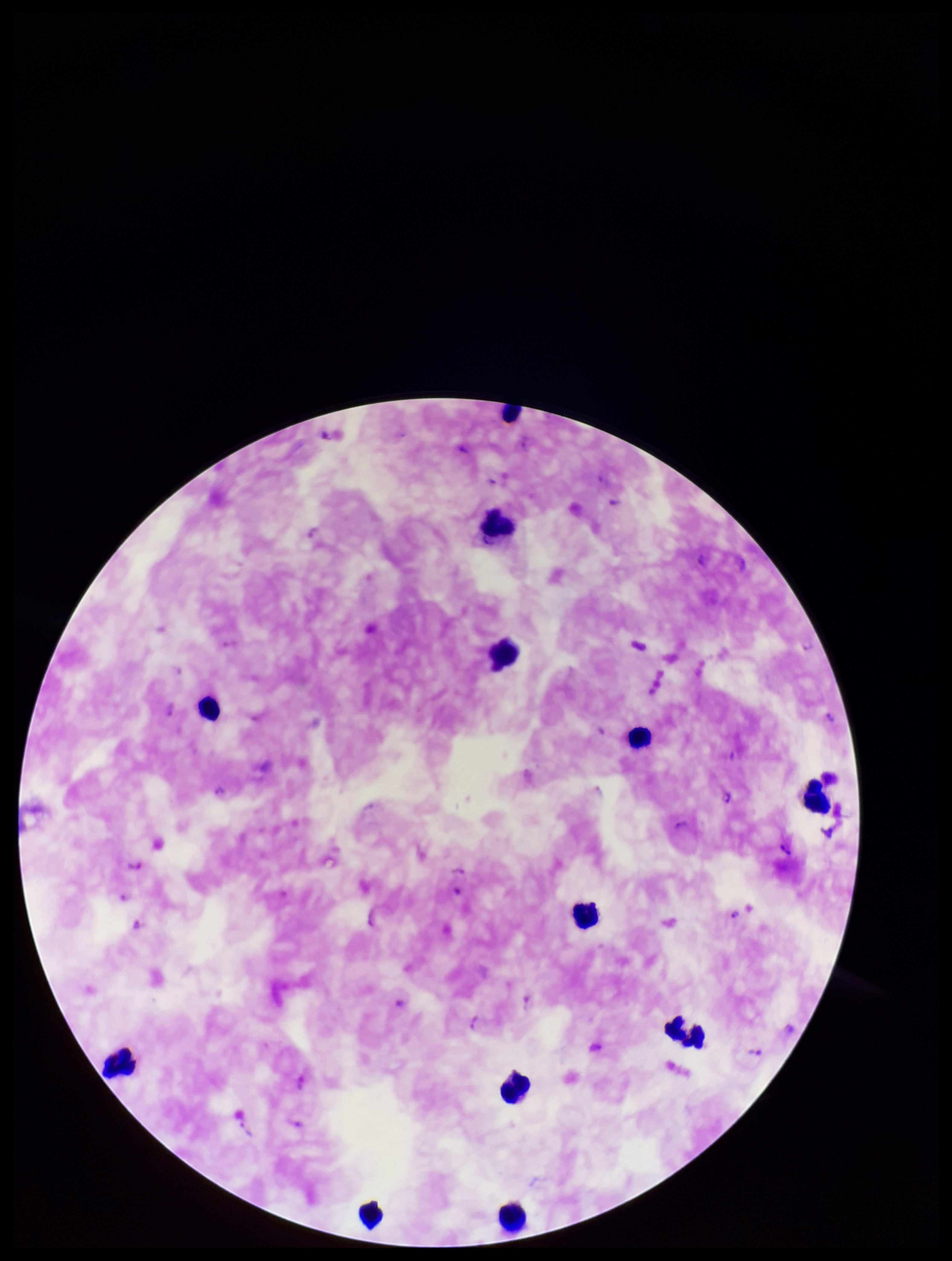

Summary:
  - Stain: Giemsa
  - Preparation: thick blood smear
  - Image size: 952×1261 pixels
  - Patient malaria status: positive
  - Field of view: one from this slide
  - Plasmodium parasites: detected
  - Parasite count: 5
  - Capture: smartphone photograph through the microscope eyepiece
  - Species reported for this patient: Plasmodium falciparum
  - Leukocyte count: 11